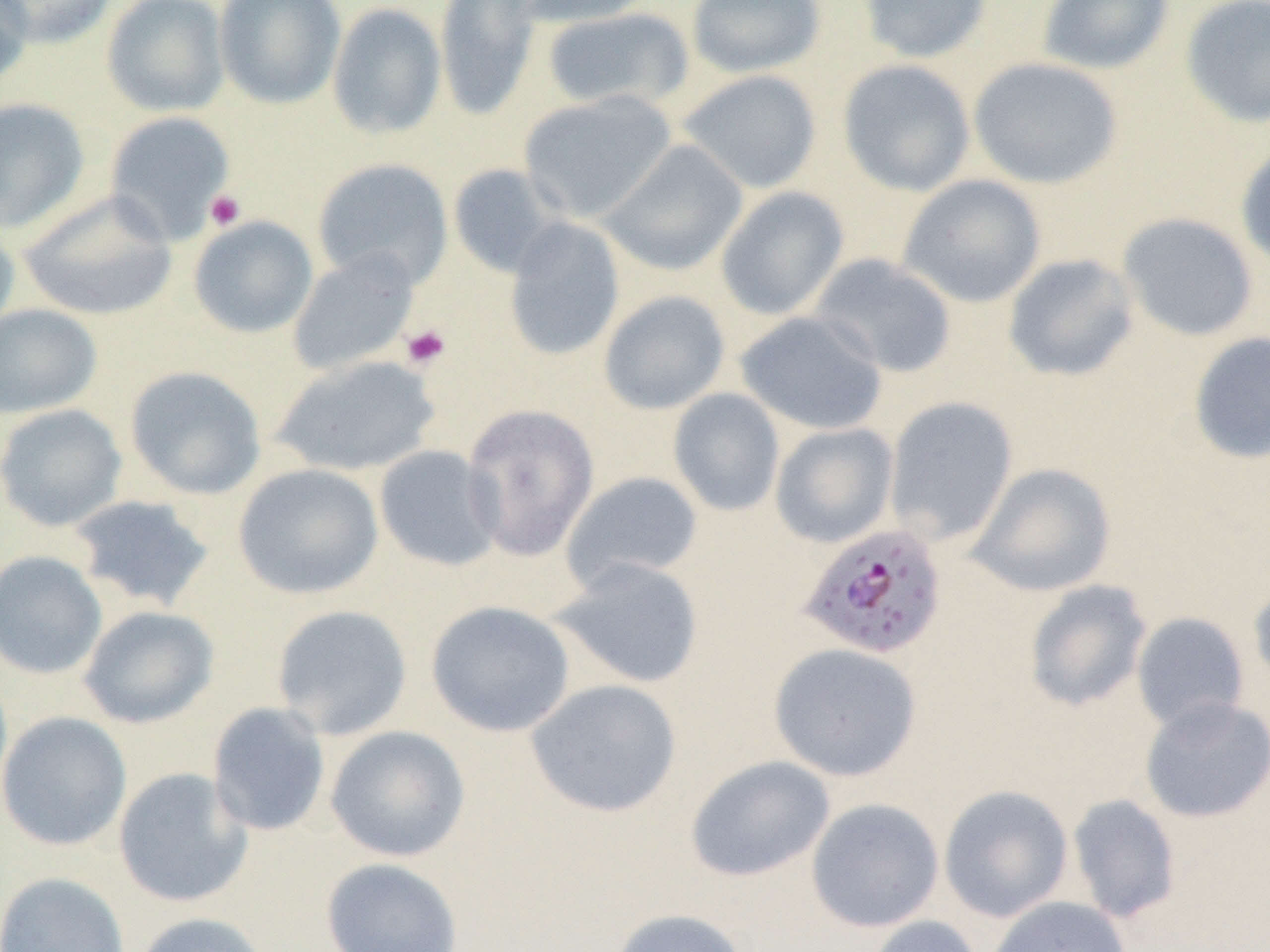 Approximate bounding boxes as [x1, y1, x2, y2] in pixels. Plasmodium falciparum-infected red blood cell locations: [795, 523, 949, 661]. Platelet locations: [204, 190, 246, 231], [401, 324, 451, 370]. Uninfected red blood cell locations: [0, 0, 33, 88], [2, 0, 116, 48], [101, 0, 230, 117], [214, 0, 346, 109], [434, 0, 543, 122], [512, 0, 655, 28], [686, 0, 826, 78], [858, 0, 993, 63], [1037, 0, 1175, 75], [1180, 0, 1270, 128], [327, 3, 447, 139], [542, 7, 694, 113], [968, 57, 1123, 189], [837, 59, 976, 197], [679, 69, 822, 194], [518, 91, 677, 223], [0, 97, 90, 233], [104, 110, 236, 244], [600, 140, 749, 276], [1235, 141, 1270, 273], [312, 157, 453, 290], [448, 163, 566, 279], [898, 174, 1047, 308], [715, 186, 849, 321], [19, 190, 178, 322], [1116, 211, 1259, 342], [188, 216, 318, 338], [503, 217, 625, 362], [0, 220, 21, 339], [287, 249, 420, 377], [809, 253, 957, 378], [1002, 253, 1140, 382], [598, 290, 730, 415], [0, 303, 102, 419], [736, 310, 888, 435], [1187, 331, 1270, 465], [270, 354, 442, 477], [124, 365, 266, 500], [668, 388, 785, 516], [884, 396, 1019, 545], [461, 402, 600, 562], [0, 403, 128, 532], [769, 422, 899, 548], [374, 445, 503, 572], [967, 462, 1117, 597], [232, 463, 384, 600], [561, 470, 703, 592], [67, 494, 217, 612], [0, 550, 107, 679], [551, 557, 705, 689], [1248, 577, 1270, 696], [1023, 580, 1152, 713], [426, 600, 576, 737], [270, 604, 413, 740], [78, 605, 219, 729], [1131, 611, 1250, 734], [768, 642, 923, 782], [525, 678, 682, 818], [1138, 696, 1269, 823], [207, 701, 331, 837], [0, 711, 133, 852], [325, 725, 471, 862], [685, 755, 835, 883], [113, 767, 253, 908], [938, 784, 1073, 922], [1067, 794, 1182, 924], [805, 797, 945, 933], [320, 857, 464, 951], [0, 871, 130, 952], [986, 896, 1132, 952], [607, 907, 751, 952], [131, 911, 272, 952], [864, 915, 984, 952]. Slide-level diagnosis: Plasmodium falciparum. Image is 1270×952 pixels. Captured at 1000x magnification. Thin blood film. Optical microscopy. One field of a larger specimen.